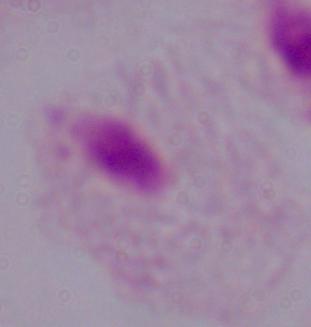
identification = trichomonad
modality = photomicrograph
magnification = 1000x